Classify this cell by malaria status.
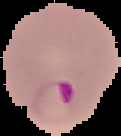

It is parasitized.

{
  "preparation": "thin blood smear",
  "image_size": "121×136 pixels",
  "image_type": "cell region segmented out of the field of view; surrounding area masked to black"
}